Identify the parasite.
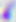
This is Toxoplasma gondii.

400x magnification. Photomicrograph.